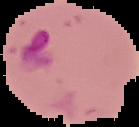

Summary:
  - Preparation: thin blood smear
  - Image type: segmented cell region with the area outside set to black
  - Malaria status: parasitized
  - Image size: 139×127 pixels